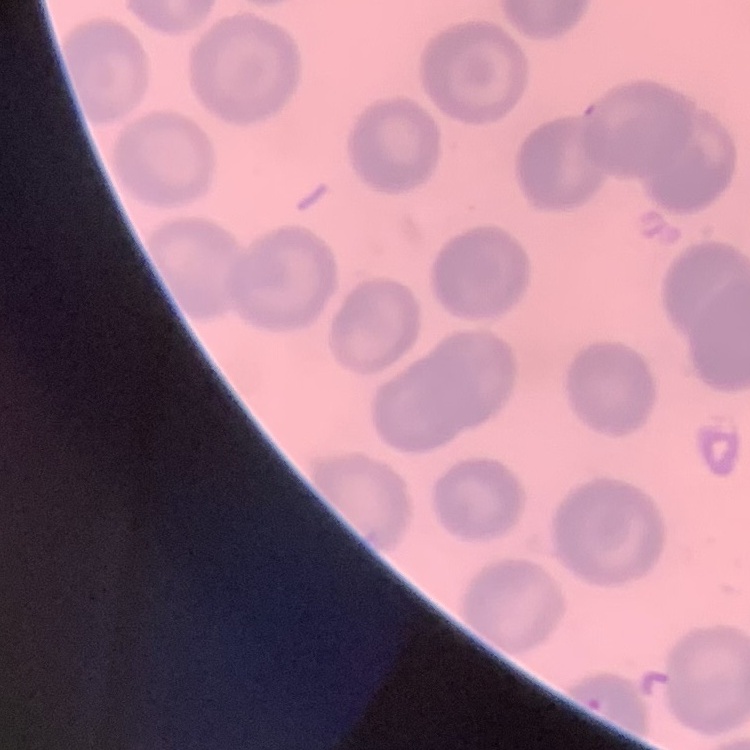
Summary:
  - Erythrocyte morphology: no rouleaux formation
  - Stain: Field's or Giemsa
  - Preparation: thin blood smear
  - Image type: one tile cut from a larger photomicrograph